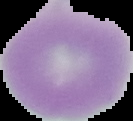

image size = 133×121 pixels
image type = segmented cell region with the area outside set to black
result = no malaria parasites seen
preparation = thin blood film